Comment on the morphology of the red blood cells.
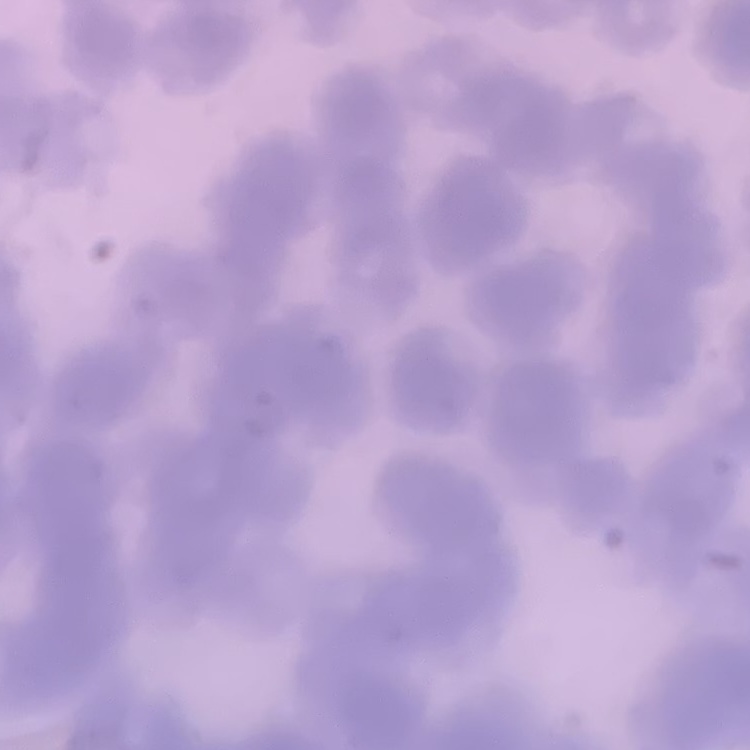

Rouleaux formation.

Summary:
  - Preparation: thin blood film
  - Image type: one tile cut from a larger photomicrograph
  - Stain: Field's or Giemsa